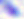

Toxoplasma gondii is shown. Micrograph. 400x magnification.